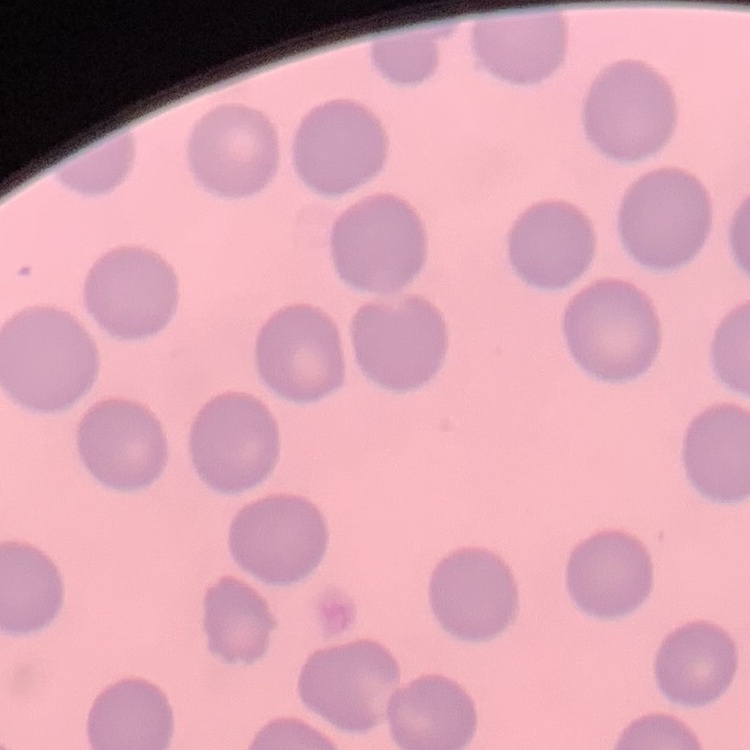

Summary:
  - Red blood cell morphology: no rouleaux formation
  - Preparation: thin blood film
  - Stain: Field's or Giemsa
  - Image type: one tile cut from a larger photomicrograph